Evaluate for Plasmodium parasites.
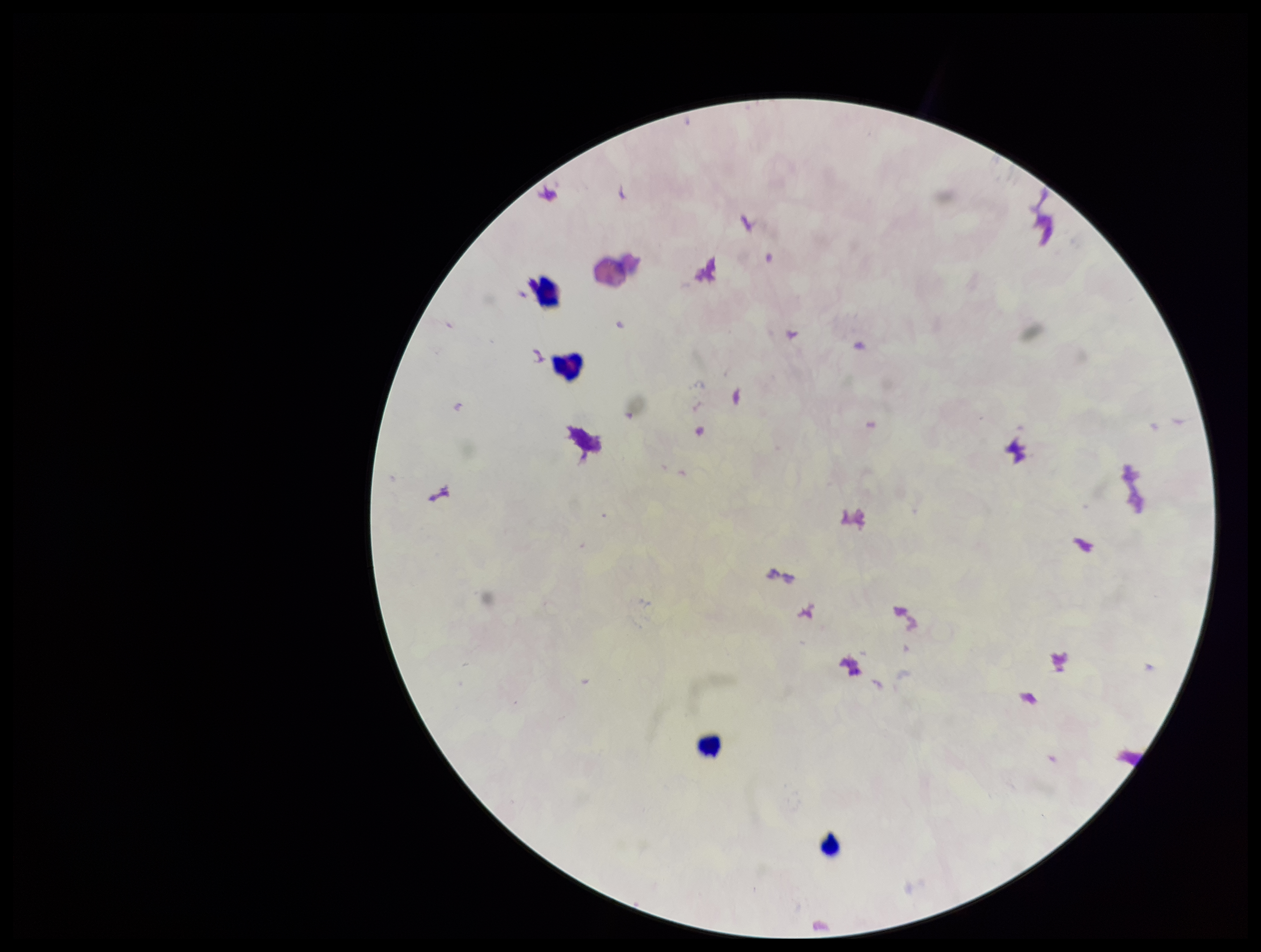

None seen.

Image is 1261×952 pixels. Parasite count: 0. Preparation: thick smear. Smartphone photograph taken through the eyepiece of a microscope. Leukocyte count: 4. Single field of view. Stained with Giemsa. Patient malaria status: negative.